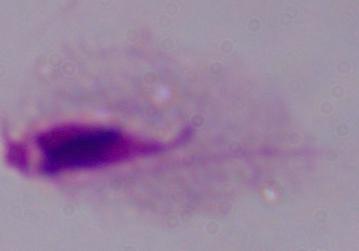
modality = micrograph
identification = trichomonad
magnification = 1000x